Locate every Plasmodium falciparum-infected red blood cell.
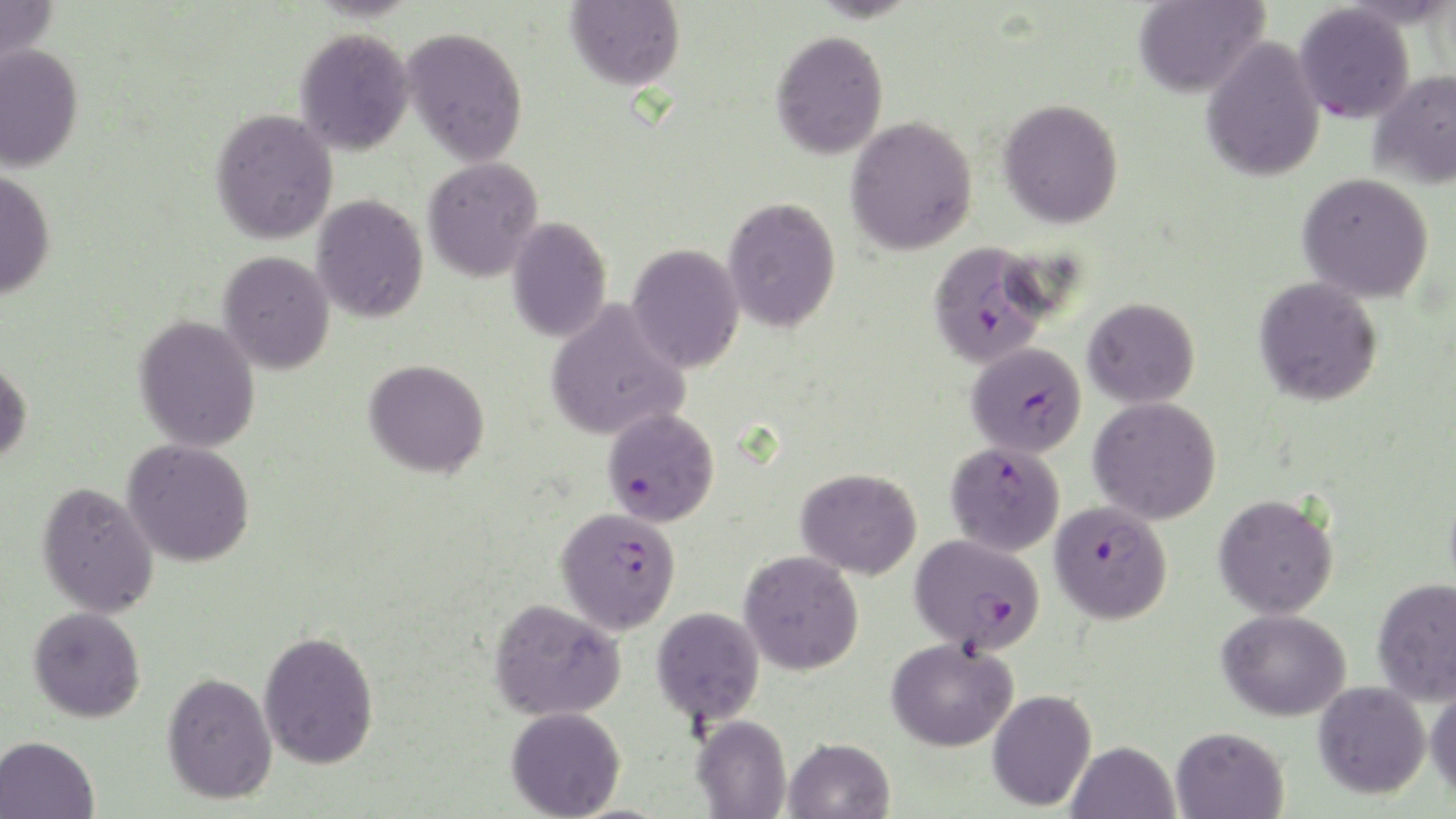
Approximate bounding boxes as [x1, y1, x2, y2] in pixels.
Plasmodium falciparum-infected red blood cells: [1294, 3, 1415, 124], [927, 240, 1055, 368], [966, 342, 1087, 458], [602, 408, 720, 528], [945, 440, 1065, 556], [1050, 500, 1172, 624], [556, 505, 681, 634], [910, 533, 1045, 654].

slide_level_diagnosis: Plasmodium falciparum
magnification: 1000x
field_of_view: single
uninfected_red_blood_cell_locations: 'approximate bounding boxes as [x1, y1, x2, y2] in pixels: [0, 0, 59, 75], [565, 0, 684, 90], [1133, 0, 1269, 98], [402, 26, 529, 166], [294, 27, 415, 155], [770, 30, 889, 160], [1201, 36, 1326, 183], [0, 43, 84, 172], [1369, 69, 1456, 189], [998, 97, 1125, 228], [210, 108, 338, 244], [846, 115, 978, 255], [422, 157, 544, 282], [0, 169, 57, 300], [1298, 172, 1434, 303], [311, 194, 429, 323], [723, 196, 841, 333], [506, 217, 612, 343], [627, 242, 745, 374], [218, 250, 335, 375], [1254, 276, 1383, 406], [1083, 297, 1200, 409], [545, 299, 691, 441], [133, 315, 261, 453], [0, 359, 33, 465], [363, 359, 489, 478], [1089, 396, 1222, 525], [122, 439, 255, 567], [796, 467, 922, 580], [36, 481, 159, 618], [1213, 492, 1339, 619], [739, 550, 864, 675], [1372, 577, 1456, 706], [489, 597, 626, 721], [28, 606, 146, 723], [652, 606, 765, 725], [1217, 608, 1352, 721], [258, 630, 380, 770], [886, 637, 1018, 752], [161, 671, 278, 804], [1313, 681, 1431, 799], [1426, 683, 1456, 799], [987, 689, 1097, 812], [506, 706, 625, 819], [691, 714, 792, 819], [1170, 726, 1289, 819], [0, 735, 99, 819], [784, 738, 895, 819], [1066, 740, 1179, 819]'
stain: May-Grünwald-Giemsa
image_size: 1456×819 pixels
preparation: thin blood film
modality: optical microscopy